Assess this cell for malaria.
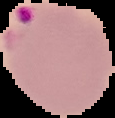

Parasitized.

Summary:
  - Image size: 115×118 pixels
  - Image type: segmented cell region with the area outside set to black
  - Preparation: thin blood film